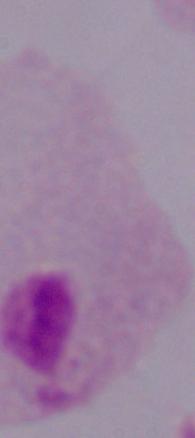
magnification = 1000x
identification = trichomonad
modality = micrograph